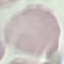
Summary:
  - Malaria status: uninfected
  - Stain: Giemsa
  - Preparation: thin smear
  - Capture: smartphone camera at the microscope eyepiece
  - Image type: automatically extracted cell patch, resized to 64 × 64 pixels